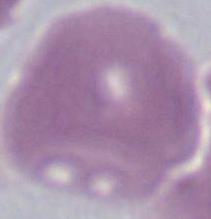
identification = erythrocyte
modality = photomicrograph
magnification = 1000x